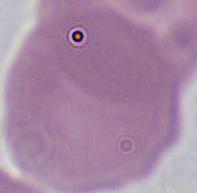
{
  "magnification": "1000x",
  "identification": "erythrocyte",
  "modality": "micrograph"
}